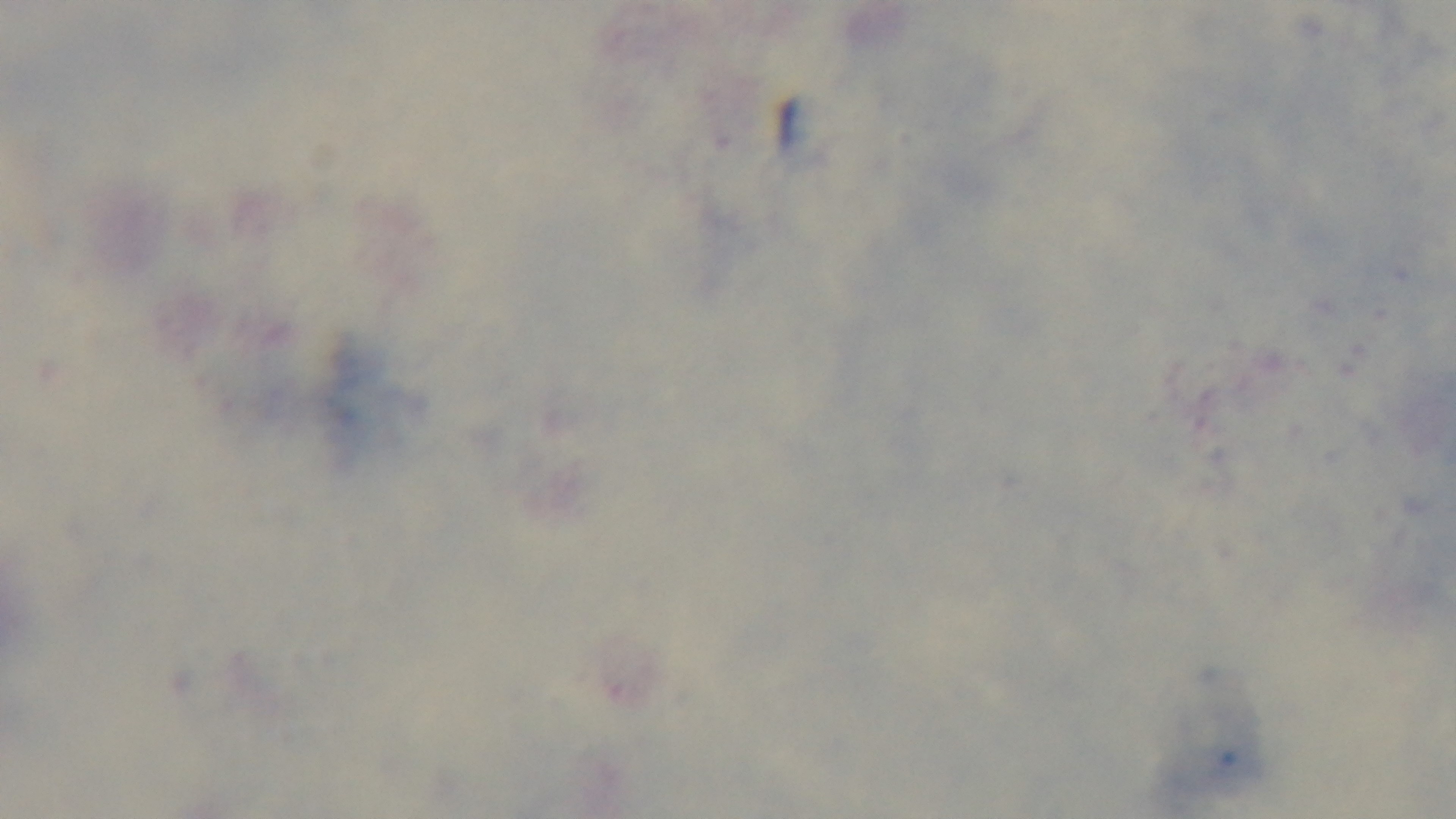

field_of_view: single
stain: Giemsa
modality: light microscopy
malaria_status: uninfected
preparation: thick
capture: mounted 4K digital camera
objective: 100x oil immersion